Describe the morphology of the red blood cells.
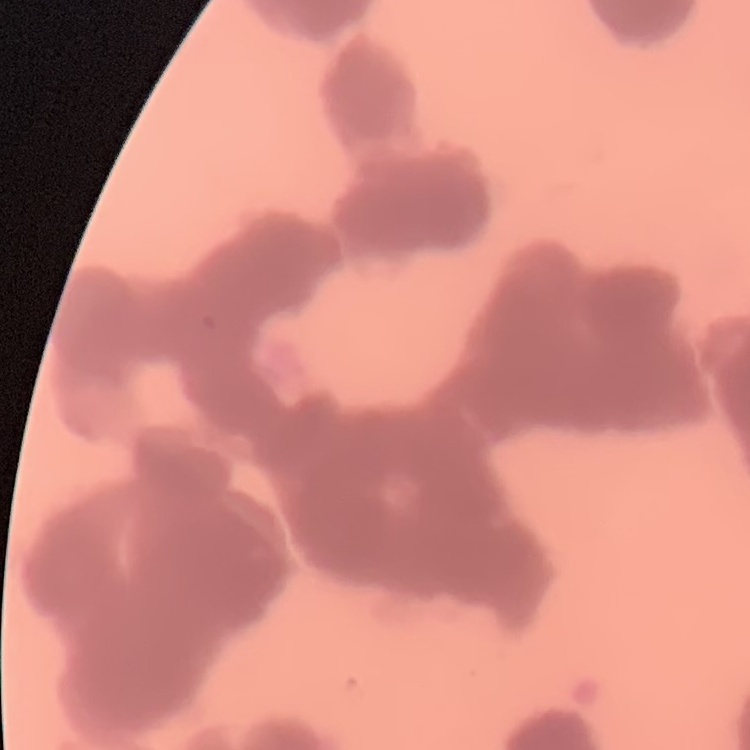
Rouleaux formation.

Thin peripheral smear. Field's or Giemsa stain. Square crop of a larger photomicrograph.